Assess for parasitized red blood cells.
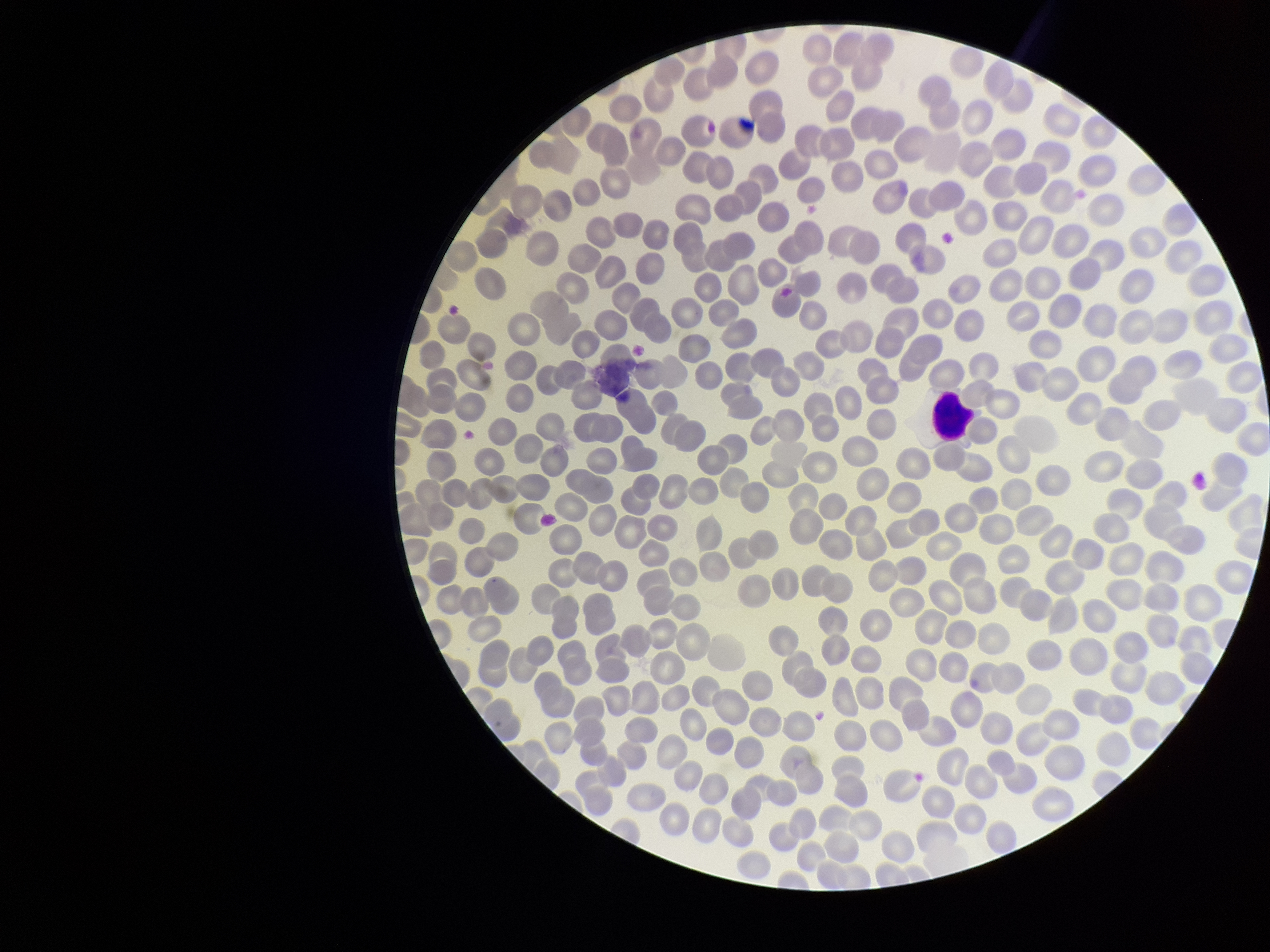

None detected.

{
  "preparation": "thin blood smear",
  "patient_malaria_status": "negative",
  "parasitized_red_blood_cell_count": 0,
  "red_blood_cell_count": 275,
  "capture": "smartphone photograph through the microscope eyepiece",
  "field_of_view": "single",
  "image_size": "1270×952 pixels",
  "stain": "Giemsa"
}